Assess the morphology of the erythrocytes.
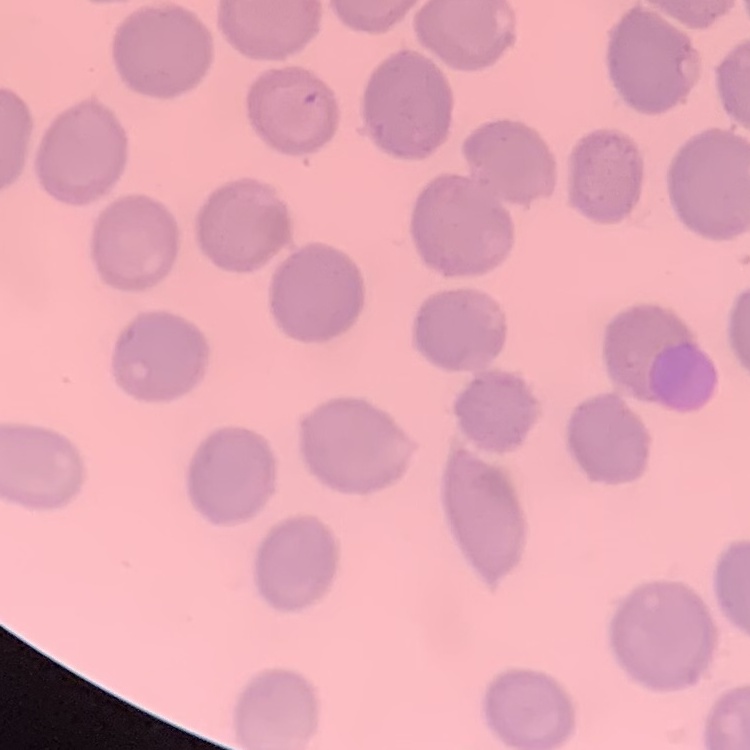

They show no rouleaux formation.

Summary:
  - Preparation: thin blood smear
  - Stain: Field's or Giemsa
  - Image type: square crop of a larger photomicrograph